Locate every Plasmodium parasite.
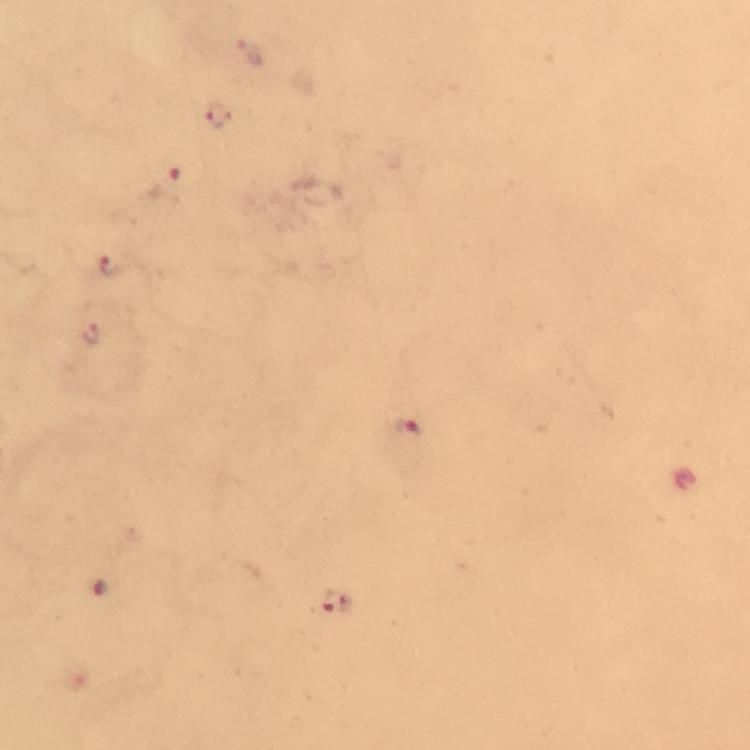
Approximate centers as {x, y} in pixels.
Plasmodium parasites: {251, 53}, {218, 115}, {170, 183}, {112, 264}, {91, 333}, {407, 431}, {100, 588}, {335, 604}.

Image is 750×750 pixels. At 100x magnification. Smartphone photograph taken through a microscope. Cropped region of a single field of view. Thick blood film. Immersion oil was used. Giemsa-stained preparation. From a diagnostic examination for malaria.